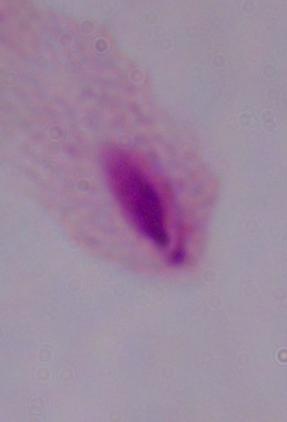

Summary:
  - Identification: trichomonad
  - Magnification: 1000x
  - Modality: photomicrograph